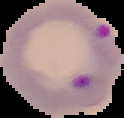

malaria status = parasitized
image type = cell region segmented out of the field of view; surrounding area masked to black
preparation = thin blood smear
image size = 124×118 pixels